Outline each blood parasite and name the species.
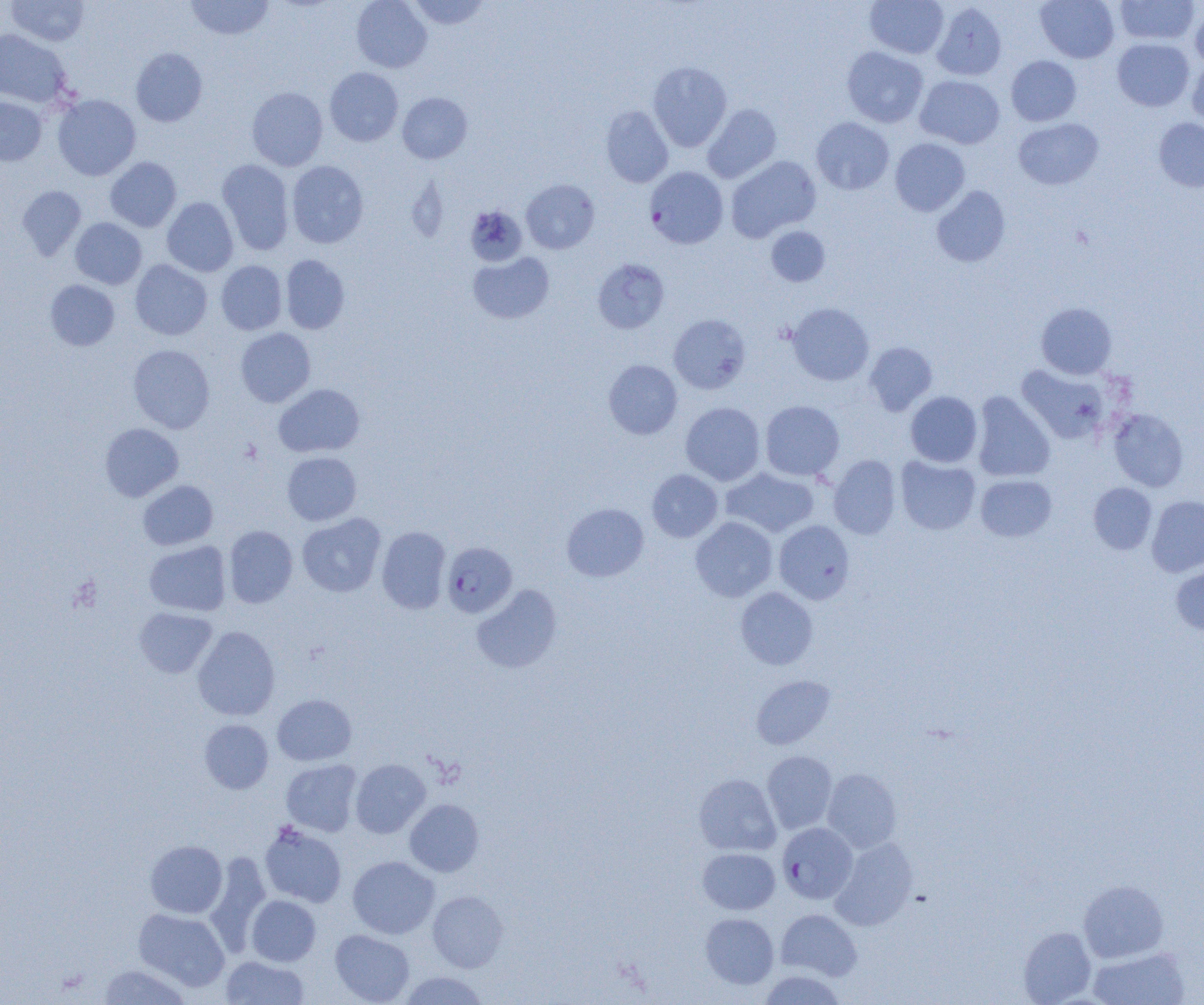

Approximate bounding boxes as [x1, y1, x2, y2] in pixels.
Plasmodium falciparum-infected red blood cells: [644, 166, 728, 248], [441, 542, 517, 618], [777, 822, 858, 903].
No Plasmodium ovale, Plasmodium malariae, Plasmodium vivax, Babesia divergens, or Trypanosoma brucei observed.

slide-level diagnosis = Plasmodium falciparum
magnification = 1000x
field of view = one of a larger specimen
preparation = thin blood film
modality = optical microscopy
image size = 1204×1005 pixels
uninfected red blood cell locations = approximate bounding boxes as [x1, y1, x2, y2] in pixels: [6, 0, 90, 46], [185, 0, 274, 40], [351, 0, 432, 73], [408, 0, 491, 30], [865, 0, 949, 59], [1036, 0, 1119, 63], [1115, 0, 1199, 45], [931, 2, 1007, 81], [1190, 6, 1204, 70], [0, 29, 72, 108], [1112, 38, 1194, 111], [841, 46, 928, 127], [131, 48, 208, 127], [1006, 55, 1081, 126], [1187, 58, 1204, 128], [648, 61, 731, 151], [325, 67, 403, 146], [915, 75, 1005, 149], [247, 87, 328, 170], [397, 92, 472, 164], [52, 94, 141, 180], [0, 96, 47, 165], [703, 103, 781, 183], [601, 105, 673, 187], [811, 117, 894, 195], [1013, 118, 1103, 189], [1154, 118, 1204, 192], [890, 138, 970, 216], [726, 156, 821, 242], [105, 157, 181, 232], [217, 159, 295, 255], [286, 161, 368, 248], [521, 179, 599, 254], [17, 185, 87, 260], [931, 186, 1010, 267], [162, 197, 238, 276], [465, 205, 527, 266], [70, 218, 147, 289], [766, 226, 830, 286], [468, 252, 554, 324], [280, 255, 350, 334], [592, 258, 669, 334], [130, 259, 212, 340], [216, 260, 287, 335], [45, 280, 120, 351], [786, 302, 874, 386], [1036, 302, 1117, 379], [669, 314, 751, 394], [235, 328, 315, 407], [863, 341, 937, 415], [128, 345, 215, 433], [603, 359, 682, 439], [1015, 364, 1111, 444], [273, 384, 365, 457], [905, 391, 983, 467], [972, 391, 1056, 482], [760, 400, 844, 481], [680, 402, 766, 485], [1108, 408, 1189, 491], [100, 423, 183, 502], [282, 452, 362, 525], [828, 454, 901, 539], [895, 455, 981, 535], [721, 467, 819, 538], [647, 469, 722, 542], [975, 474, 1057, 541], [138, 480, 218, 550], [1088, 482, 1157, 554], [1146, 495, 1204, 577], [562, 503, 649, 581], [297, 513, 386, 597], [690, 516, 777, 602], [774, 520, 855, 604], [224, 525, 298, 608], [377, 526, 451, 614], [144, 541, 231, 616], [1170, 562, 1204, 637], [471, 584, 562, 673], [735, 586, 818, 669], [134, 607, 217, 678], [193, 625, 280, 720], [751, 675, 836, 750], [272, 694, 356, 766], [199, 719, 273, 793], [762, 751, 837, 834], [281, 759, 363, 837], [350, 759, 430, 838], [822, 768, 902, 853], [694, 773, 781, 856], [405, 799, 484, 877], [259, 822, 347, 908], [830, 837, 918, 930], [145, 840, 227, 917], [698, 847, 780, 914], [205, 852, 271, 952], [348, 856, 440, 939], [1079, 879, 1169, 963], [428, 891, 508, 972], [246, 895, 321, 966], [133, 908, 230, 991], [776, 909, 862, 980], [700, 913, 779, 989], [1018, 926, 1096, 1004], [330, 929, 414, 1004], [1087, 946, 1190, 1005], [221, 955, 309, 1004], [97, 963, 192, 1004], [758, 970, 846, 1004], [399, 971, 489, 1004]